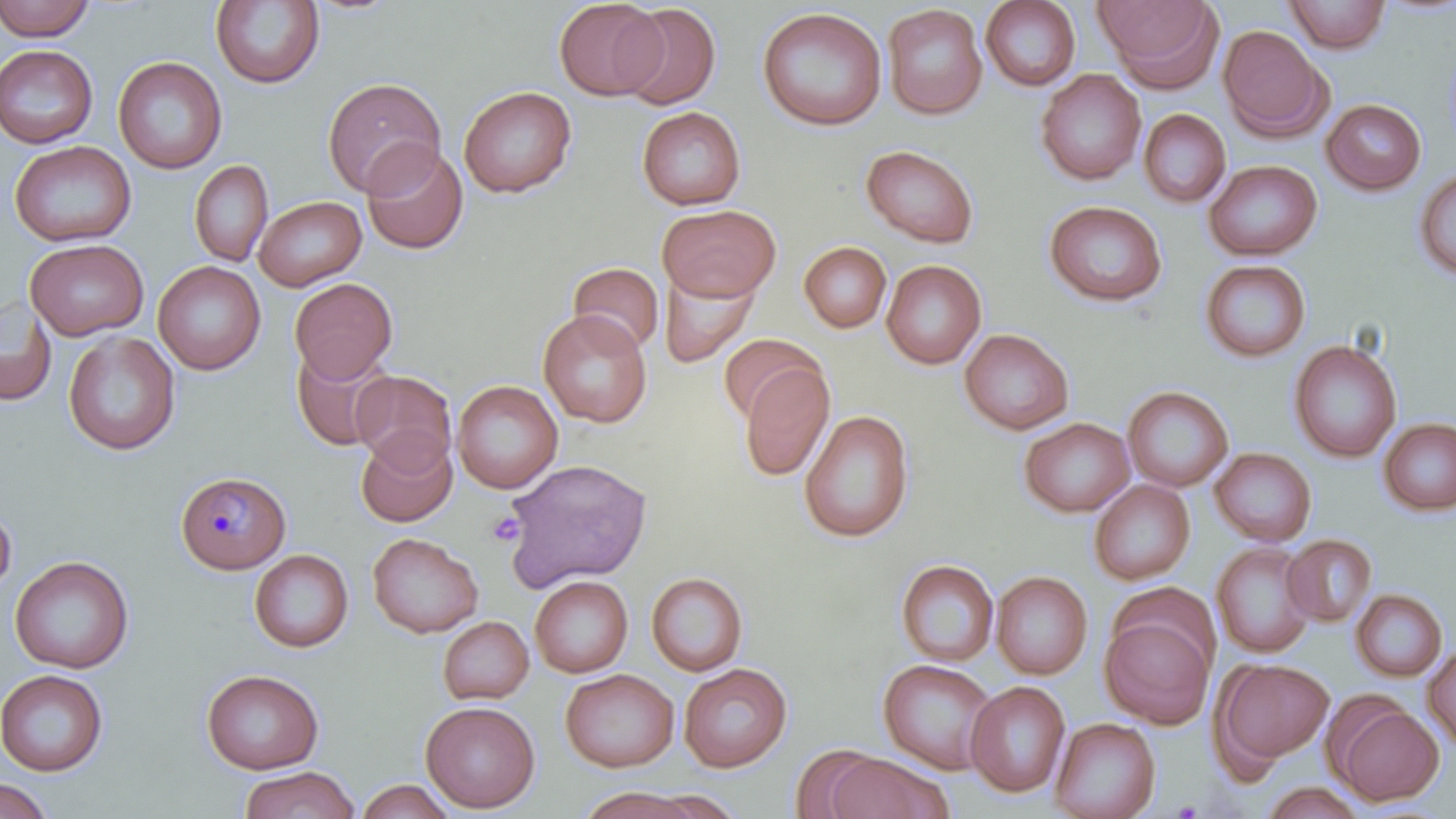

Approximate bounding boxes as (x1,y1)-(x2,y2) corner pairs in pixels. Uninfected red blood cell locations: (0,0)-(96,42), (210,0)-(325,89), (554,0)-(667,101), (980,0)-(1081,91), (1093,0)-(1224,91), (1283,0)-(1391,54), (616,4)-(721,111), (882,4)-(988,120), (756,6)-(887,131), (1218,24)-(1332,141), (0,44)-(98,149), (113,56)-(227,174), (1035,69)-(1146,186), (322,77)-(446,197), (458,85)-(577,198), (1321,98)-(1427,195), (636,106)-(746,210), (1138,108)-(1231,209), (9,140)-(136,247), (361,143)-(468,255), (861,144)-(979,248), (189,159)-(273,267), (1204,159)-(1322,261), (1413,168)-(1456,282), (253,195)-(366,291), (1043,200)-(1168,307), (656,204)-(782,302), (25,238)-(149,340), (799,242)-(892,333), (881,259)-(986,369), (1199,259)-(1311,363), (153,261)-(266,375), (568,262)-(664,356), (658,268)-(759,368), (289,277)-(398,383), (0,295)-(57,407), (538,309)-(653,428), (959,328)-(1074,435), (63,331)-(181,455), (717,333)-(823,425), (1288,339)-(1402,463), (290,342)-(396,451), (738,361)-(835,482), (350,369)-(457,471), (452,380)-(563,494), (1123,385)-(1234,492), (799,409)-(915,543), (1019,417)-(1135,518), (1378,417)-(1456,517), (355,428)-(458,528), (1209,447)-(1317,546), (502,457)-(652,591), (1088,479)-(1195,585), (0,500)-(17,599), (367,532)-(483,637), (1282,534)-(1378,627), (1210,542)-(1317,658), (249,548)-(354,653), (10,555)-(134,673), (896,559)-(999,667), (646,571)-(749,676), (991,571)-(1093,680), (529,575)-(633,677), (1350,588)-(1447,681), (1100,612)-(1216,729), (437,616)-(534,705), (1422,646)-(1456,749), (877,658)-(998,775), (1212,658)-(1334,767), (679,663)-(792,773), (200,668)-(325,774), (560,668)-(679,772), (0,669)-(108,776), (965,680)-(1071,798), (420,700)-(540,812), (1329,701)-(1444,806), (1050,716)-(1161,819), (788,743)-(889,818), (824,752)-(949,819), (239,765)-(360,819), (0,777)-(53,819), (355,778)-(455,818), (1260,782)-(1370,818), (575,787)-(708,819). Plasmodium malariae-infected red blood cell locations: (175,470)-(291,575). Platelet locations: (487,511)-(525,547). Slide-level diagnosis: Plasmodium malariae. Single field of view. Optical microscopy. Image is 1456×819 pixels. Captured at 1000x magnification. Thin blood film. May-Grünwald-Giemsa-stained preparation.